Report the malaria status of this cell.
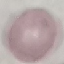
It is uninfected.

Summary:
  - Preparation: thin blood film
  - Stain: Giemsa
  - Image type: automatically extracted cell patch, resized to 64 × 64 pixels
  - Capture: smartphone through the microscope eyepiece